Assess the morphology of the erythrocytes.
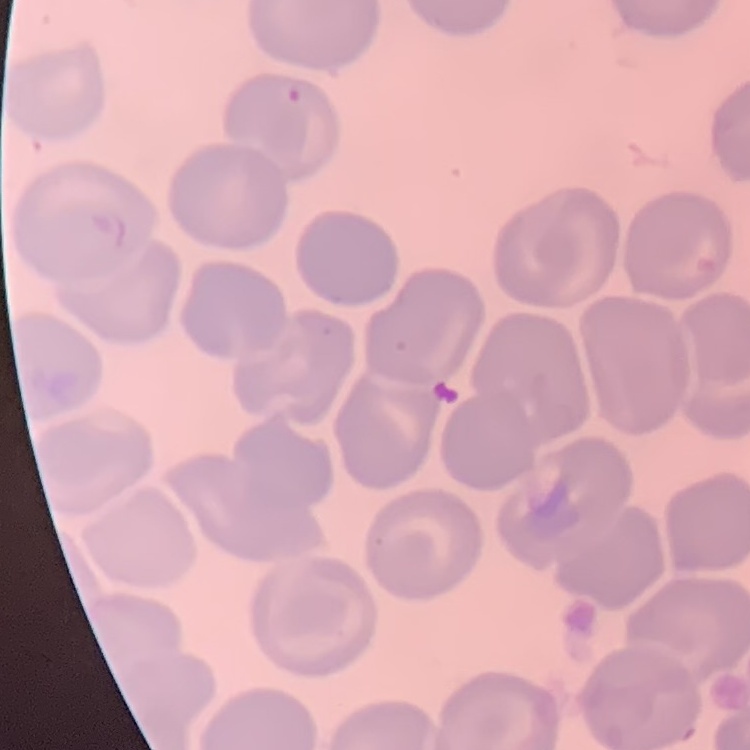
No rouleaux formation.

One tile cut from a larger photomicrograph. Thin peripheral smear. Stained with either Field's or Giemsa.